Describe the morphology of the erythrocytes.
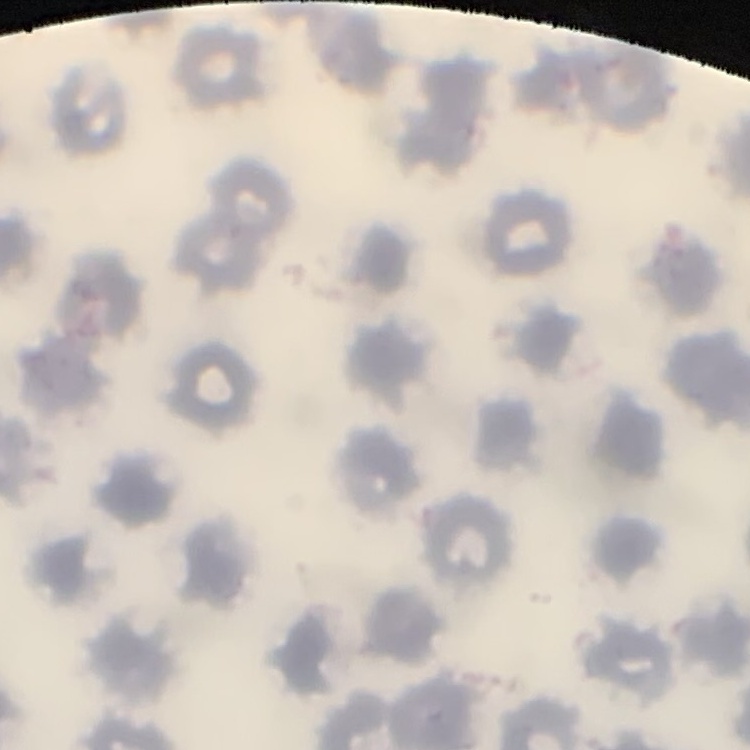
No rouleaux formation.

image type = square crop of a larger photomicrograph
stain = Field's or Giemsa
preparation = thin peripheral smear